Describe the morphology of the red blood cells.
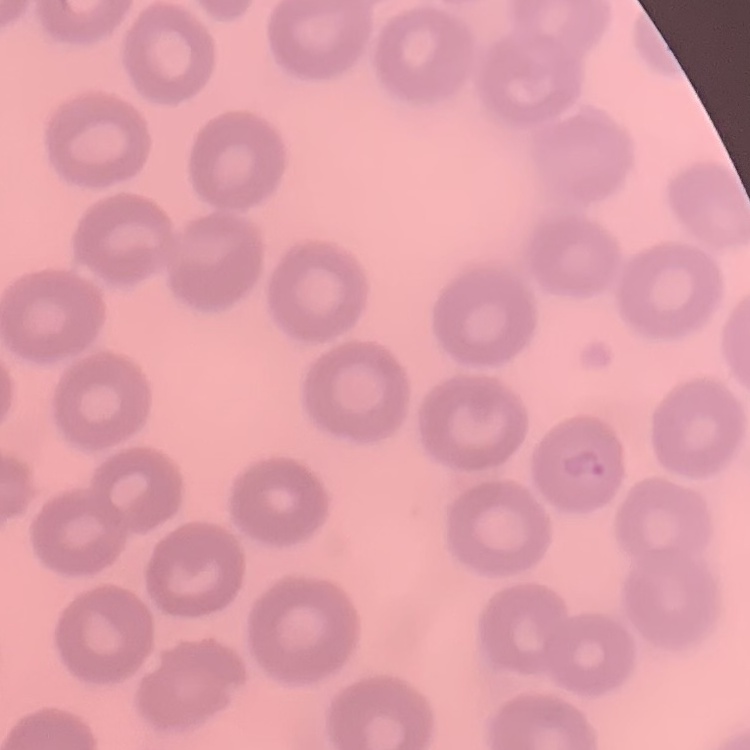
No rouleaux formation.

preparation = thin blood film
stain = Field's or Giemsa
image type = square crop of a larger photomicrograph